Identify the blood parasite species.
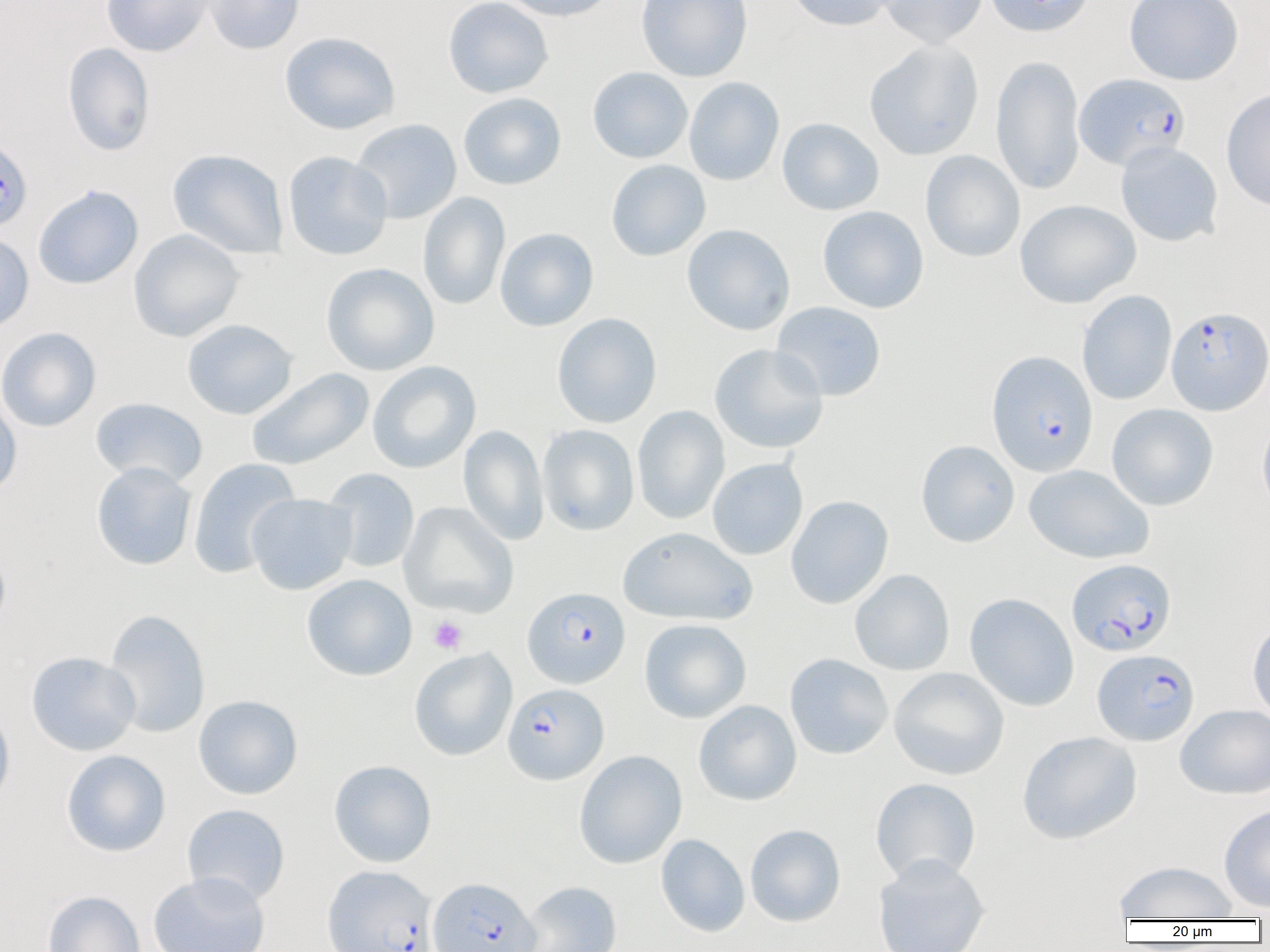

Plasmodium falciparum.

Approximate bounding boxes as (x1, y1, x2, y2) in pixels. Platelet locations: (428, 616, 467, 654). Uninfected red blood cell locations: (101, 0, 215, 57), (204, 0, 305, 55), (442, 0, 553, 99), (497, 0, 618, 21), (636, 0, 753, 82), (785, 0, 898, 31), (878, 0, 988, 48), (984, 0, 1095, 37), (1124, 0, 1244, 85), (279, 32, 401, 135), (864, 39, 984, 161), (62, 42, 156, 156), (990, 54, 1085, 195), (587, 66, 692, 164), (684, 77, 784, 186), (1221, 89, 1270, 212), (457, 92, 567, 190), (777, 117, 884, 216), (351, 118, 462, 224), (1116, 141, 1224, 247), (168, 148, 289, 259), (920, 150, 1025, 262), (283, 151, 393, 260), (605, 159, 711, 261), (33, 185, 143, 290), (418, 192, 510, 311), (1015, 199, 1141, 308), (818, 205, 928, 313), (682, 224, 795, 335), (495, 227, 599, 331), (129, 229, 245, 342), (0, 231, 34, 333), (321, 262, 439, 375), (1077, 290, 1177, 405), (771, 301, 886, 402), (552, 313, 662, 428), (182, 319, 298, 419), (0, 327, 101, 432), (709, 343, 829, 454), (368, 361, 481, 473), (246, 368, 374, 471), (0, 394, 22, 499), (90, 397, 208, 487), (1106, 403, 1218, 511), (632, 405, 730, 525), (1257, 412, 1270, 520), (538, 424, 639, 536), (458, 425, 549, 545), (916, 440, 1020, 547), (188, 457, 300, 578), (707, 458, 808, 560), (91, 461, 196, 570), (1023, 464, 1154, 564), (322, 468, 419, 573), (246, 493, 356, 595), (786, 495, 893, 609), (399, 502, 519, 618), (618, 526, 756, 625), (0, 547, 11, 638), (849, 569, 955, 675), (302, 574, 417, 681), (965, 593, 1079, 711), (104, 609, 210, 738), (1248, 617, 1270, 724), (639, 619, 751, 723), (409, 648, 517, 761), (26, 651, 140, 756), (784, 654, 893, 760), (889, 667, 1010, 780), (193, 695, 303, 799), (0, 699, 15, 811), (694, 700, 802, 806), (1175, 704, 1270, 799), (1016, 730, 1142, 845), (61, 749, 171, 857), (574, 750, 687, 869), (329, 759, 437, 868), (870, 777, 981, 885), (182, 804, 289, 906), (1218, 804, 1270, 913), (745, 824, 846, 927), (656, 834, 750, 937), (873, 854, 990, 952), (1113, 860, 1238, 920), (148, 871, 270, 952), (518, 881, 622, 952), (42, 890, 146, 952). Plasmodium falciparum-infected red blood cell locations: (1074, 73, 1189, 171), (0, 136, 33, 232), (1166, 305, 1269, 416), (986, 351, 1098, 477), (1066, 558, 1177, 657), (522, 586, 630, 688), (1092, 649, 1200, 746), (502, 683, 609, 784), (322, 865, 437, 952), (427, 878, 540, 952). Thin blood smear. Light microscopy. Captured at 1000x magnification. One field of a larger specimen. Image is 1270×952 pixels.